Assess this cell for malaria.
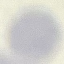

It is uninfected.

Photographed with a smartphone camera at the microscope eyepiece. Automatically extracted cell patch, resized to 64 × 64 pixels. Giemsa-stained preparation. Thin smear of blood.